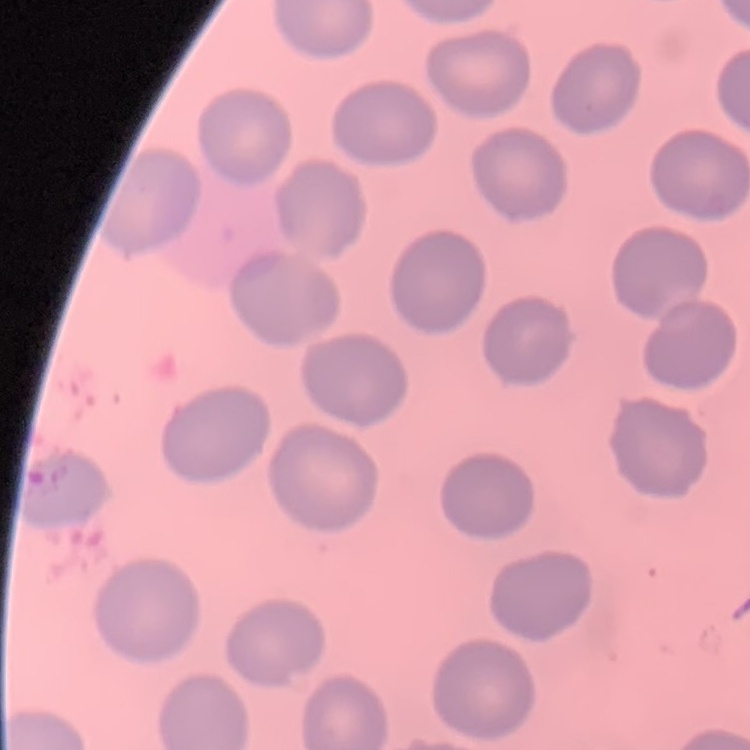

Summary:
  - Erythrocyte morphology: no rouleaux formation
  - Preparation: thin peripheral smear
  - Image type: one tile cut from a larger photomicrograph
  - Stain: Field's or Giemsa